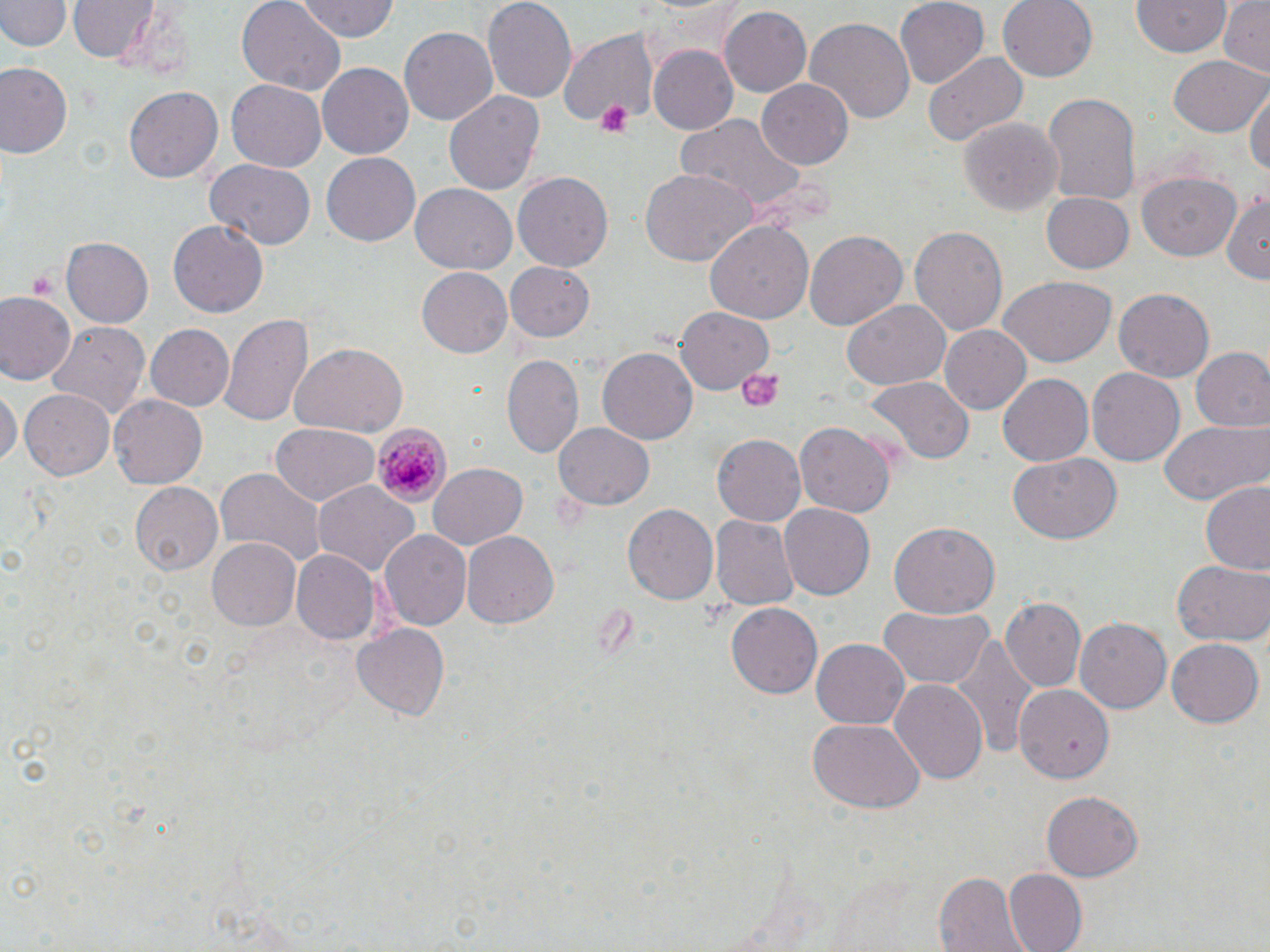
Summary:
  - Coordinate format: approximate bounding boxes as (x1, y1, x2, y2) in pixels
  - Uninfected red blood cell locations: (69, 0, 159, 65), (237, 0, 344, 98), (291, 0, 401, 42), (481, 0, 578, 105), (895, 0, 990, 89), (997, 0, 1100, 81), (1219, 0, 1270, 76), (0, 1, 67, 53), (1131, 1, 1230, 59), (719, 6, 811, 98), (806, 15, 914, 126), (400, 27, 498, 126), (553, 27, 660, 130), (646, 45, 738, 135), (924, 51, 1030, 144), (1170, 56, 1268, 137), (0, 64, 73, 159), (318, 64, 412, 158), (226, 78, 326, 170), (757, 79, 852, 169), (125, 85, 224, 183), (1246, 87, 1270, 186), (444, 90, 544, 197), (1040, 91, 1142, 209), (675, 114, 804, 215), (959, 117, 1064, 216), (322, 155, 420, 246), (203, 159, 315, 249), (638, 169, 760, 267), (513, 170, 613, 268), (1138, 171, 1244, 261), (411, 185, 516, 273), (1040, 192, 1135, 275), (1221, 192, 1270, 282), (169, 220, 268, 317), (704, 221, 814, 324), (911, 226, 1008, 341), (804, 229, 907, 332), (61, 238, 153, 326), (504, 262, 594, 343), (418, 267, 513, 358), (998, 276, 1116, 368), (1114, 288, 1215, 382), (0, 292, 77, 388), (841, 300, 949, 392), (675, 304, 774, 394), (219, 309, 314, 431), (46, 320, 150, 421), (940, 324, 1031, 416), (147, 326, 234, 411), (290, 343, 408, 437), (1191, 346, 1270, 434), (597, 349, 696, 445), (503, 356, 584, 458), (1086, 367, 1184, 466), (998, 373, 1096, 466), (865, 376, 976, 465), (1, 386, 19, 471), (21, 389, 113, 481), (107, 393, 209, 491), (1157, 420, 1270, 506), (551, 421, 654, 511), (796, 421, 894, 517), (269, 423, 380, 505), (711, 433, 807, 526), (1008, 453, 1122, 546), (425, 462, 527, 550), (217, 471, 325, 564), (312, 480, 418, 580), (131, 482, 221, 577), (1199, 482, 1270, 576), (624, 502, 719, 605), (780, 503, 875, 600), (710, 516, 797, 612), (889, 523, 999, 617), (379, 529, 471, 633), (463, 530, 558, 629), (206, 539, 303, 631), (293, 551, 379, 646), (1172, 560, 1270, 648), (1000, 598, 1085, 693), (725, 604, 820, 698), (879, 604, 993, 689), (1075, 618, 1170, 714), (353, 624, 450, 720), (953, 632, 1038, 764), (1167, 636, 1263, 725), (812, 639, 908, 727), (889, 679, 988, 786), (1014, 682, 1112, 782), (805, 717, 923, 813), (1040, 792, 1141, 882), (1003, 869, 1087, 952), (934, 872, 1024, 952)
  - Plasmodium malariae-infected red blood cell locations: (373, 423, 452, 508)
  - Platelet locations: (593, 99, 637, 140), (27, 270, 60, 301), (736, 368, 783, 413)
  - Slide-level diagnosis: Plasmodium malariae
  - Modality: optical microscopy
  - Magnification: 1000x
  - Preparation: thin blood film
  - Stain: May-Grünwald-Giemsa
  - Field of view: one of a larger specimen
  - Image size: 1270×952 pixels